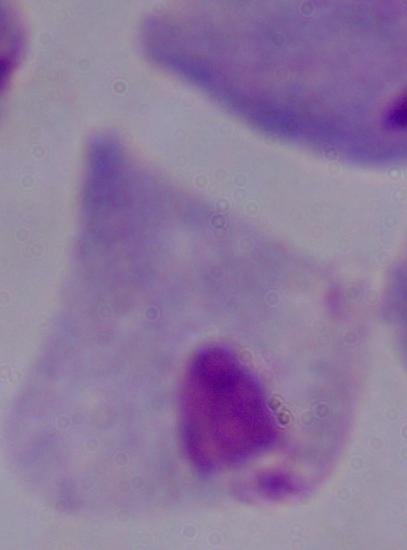
Summary:
  - Magnification: 1000x
  - Identification: trichomonad
  - Modality: micrograph